Describe the morphology of the red blood cells.
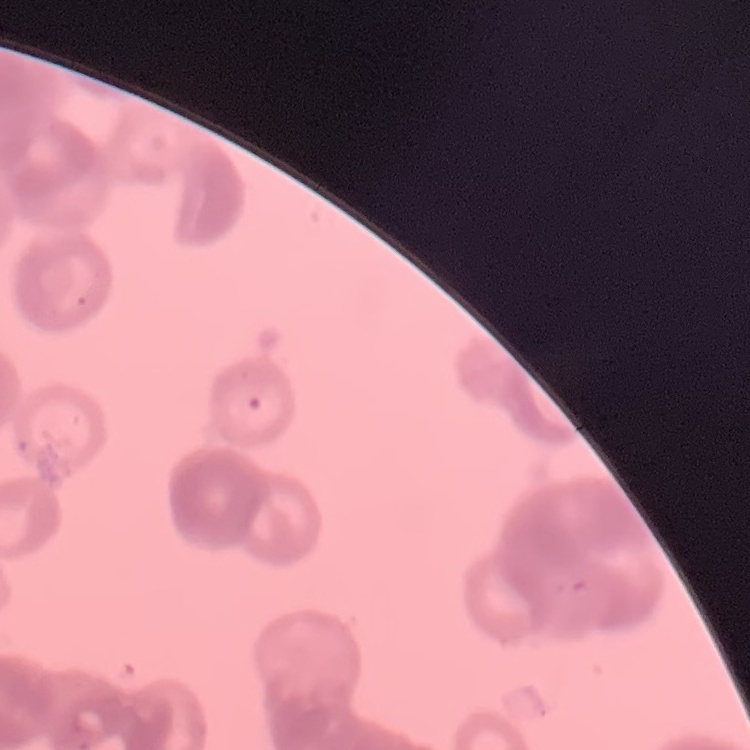

They show rouleaux formation.

Thin blood smear. One tile cut from a larger photomicrograph. Stained with either Field's or Giemsa.